Locate and identify every blood parasite.
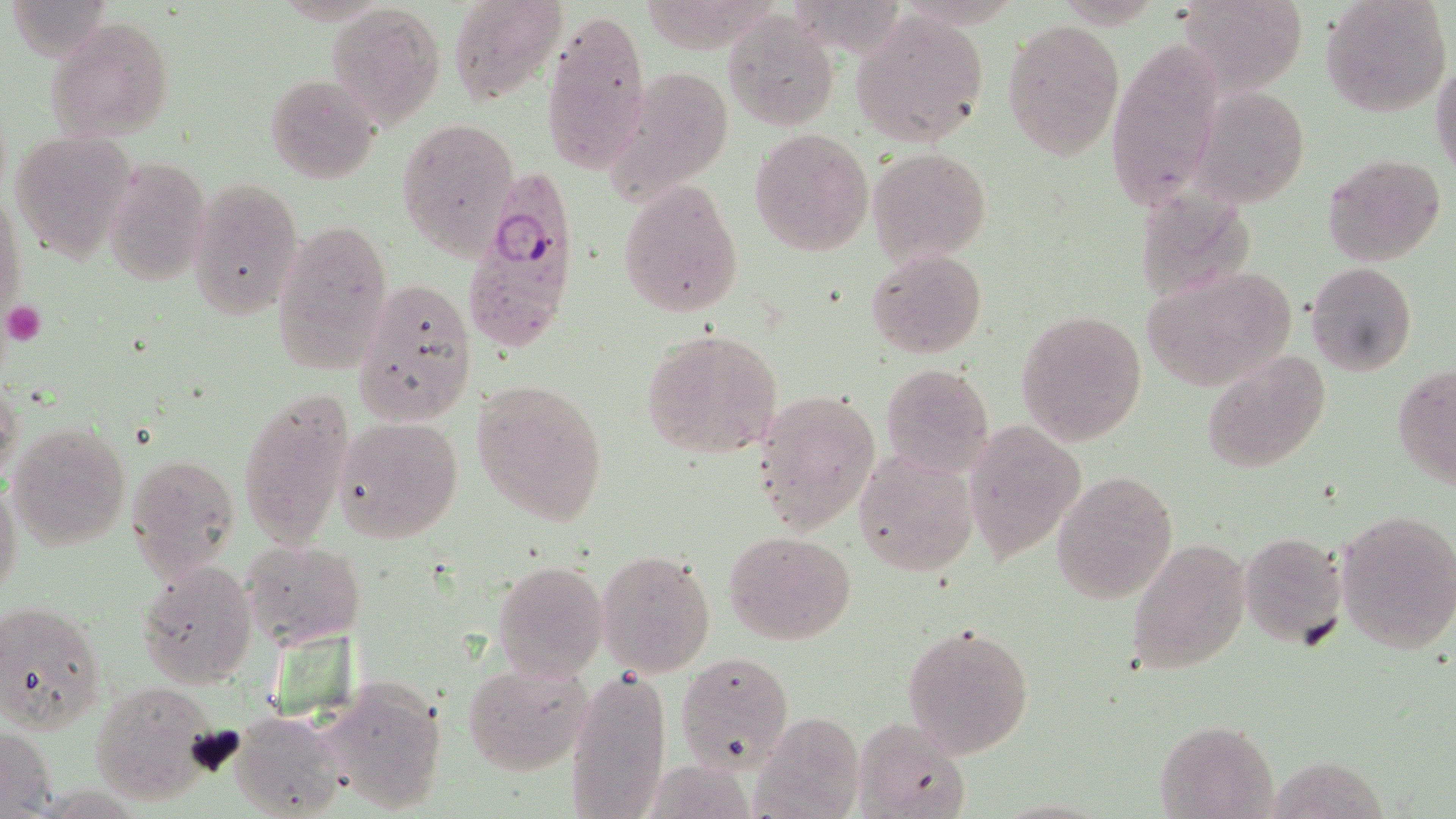

Approximate bounding boxes as [x1, y1, x2, y2] in pixels.
Plasmodium falciparum-infected red blood cells: [463, 181, 578, 354].
No Plasmodium ovale, Plasmodium malariae, Plasmodium vivax, Babesia divergens, or Trypanosoma brucei observed.

Summary:
  - Platelet locations: [1, 301, 46, 345]
  - Uninfected red blood cell locations: [9, 0, 110, 62], [446, 0, 566, 104], [1176, 0, 1309, 95], [1319, 0, 1452, 117], [326, 2, 445, 129], [724, 10, 839, 130], [541, 11, 650, 173], [854, 12, 988, 143], [46, 17, 174, 141], [1002, 20, 1125, 160], [1107, 41, 1223, 214], [1430, 60, 1456, 179], [264, 73, 380, 183], [1192, 88, 1312, 205], [398, 117, 519, 258], [748, 128, 873, 256], [10, 132, 134, 265], [869, 146, 991, 263], [1322, 153, 1447, 267], [104, 157, 211, 285], [189, 177, 304, 321], [618, 179, 744, 317], [0, 186, 25, 332], [1132, 188, 1258, 300], [270, 216, 396, 378], [868, 248, 987, 358], [1305, 262, 1417, 378], [1142, 266, 1295, 391], [353, 276, 474, 424], [1015, 309, 1148, 448], [642, 327, 784, 459], [1200, 352, 1331, 475], [879, 363, 994, 478], [1393, 364, 1456, 487], [0, 375, 23, 484], [470, 379, 610, 526], [237, 387, 358, 554], [753, 388, 881, 535], [334, 416, 465, 544], [962, 420, 1087, 562], [7, 423, 130, 550], [853, 449, 978, 578], [126, 451, 243, 582], [1052, 471, 1178, 605], [0, 477, 22, 603], [1334, 509, 1456, 655], [725, 530, 856, 644], [1238, 532, 1347, 650], [1125, 537, 1250, 675], [242, 539, 366, 648], [596, 549, 717, 677], [138, 560, 259, 689], [492, 561, 608, 682], [0, 599, 106, 734], [901, 621, 1036, 759], [677, 651, 794, 771], [462, 660, 593, 776], [565, 664, 673, 819], [315, 677, 451, 817], [87, 682, 222, 805], [231, 709, 347, 818], [752, 711, 866, 818], [851, 715, 973, 819], [1156, 719, 1277, 818], [0, 727, 59, 817], [1267, 755, 1390, 819]
  - Slide-level diagnosis: Plasmodium falciparum
  - Field of view: single
  - Magnification: 1000x
  - Modality: light microscopy
  - Image size: 1456×819 pixels
  - Preparation: thin blood smear
  - Stain: May-Grünwald-Giemsa